Report the malaria status of this cell.
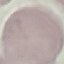
Uninfected.

stain = Giemsa
preparation = thin blood film
capture = smartphone through the microscope eyepiece
image type = automatically extracted cell patch, resized to 64 × 64 pixels